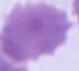
Summary:
  - Magnification: 1000x
  - Modality: photomicrograph
  - Identification: red blood cell